Comment on the morphology of the erythrocytes.
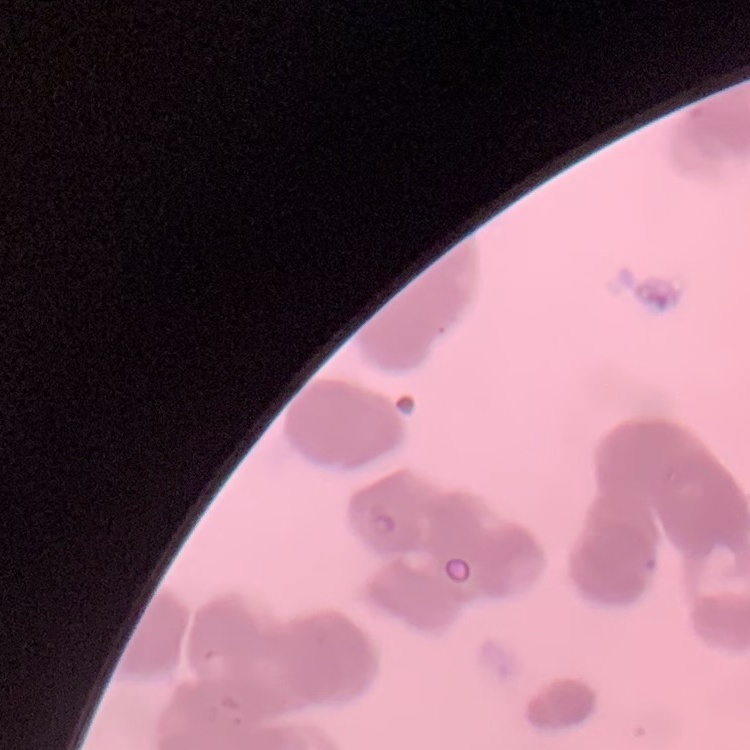

They show rouleaux formation.

Stained with either Field's or Giemsa. One tile cut from a larger photomicrograph. Thin blood smear.